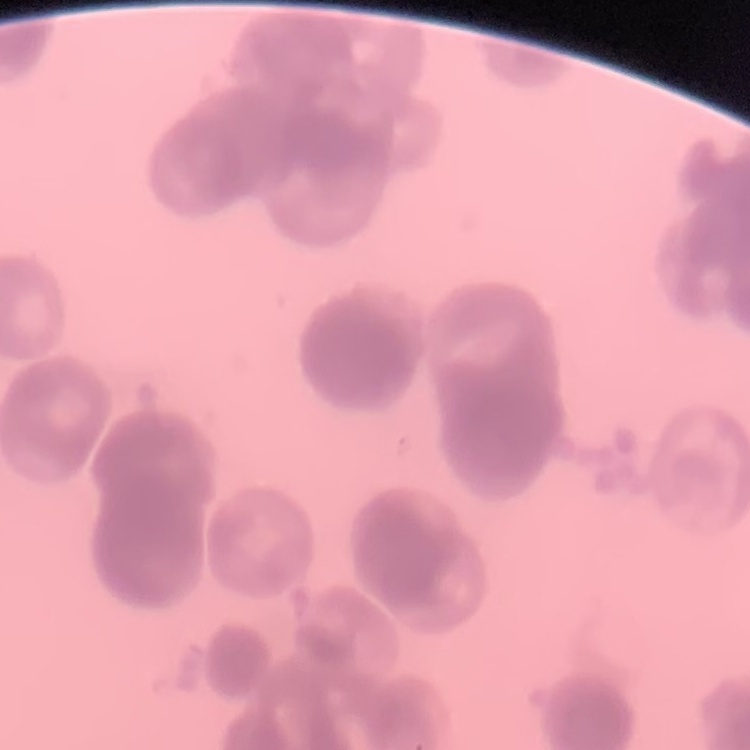
erythrocyte morphology = rouleaux formation
preparation = thin peripheral smear
stain = Field's or Giemsa
image type = one tile cut from a larger photomicrograph